Report the malaria status of this cell.
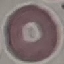
Uninfected.

Summary:
  - Stain: Giemsa
  - Image type: automatically extracted cell patch, resized to 64 × 64 pixels
  - Preparation: thin blood film
  - Capture: smartphone camera at the microscope eyepiece